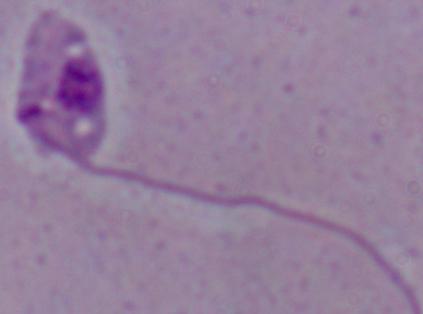

A Leishmania parasite is seen. Photomicrograph. 1000x magnification.